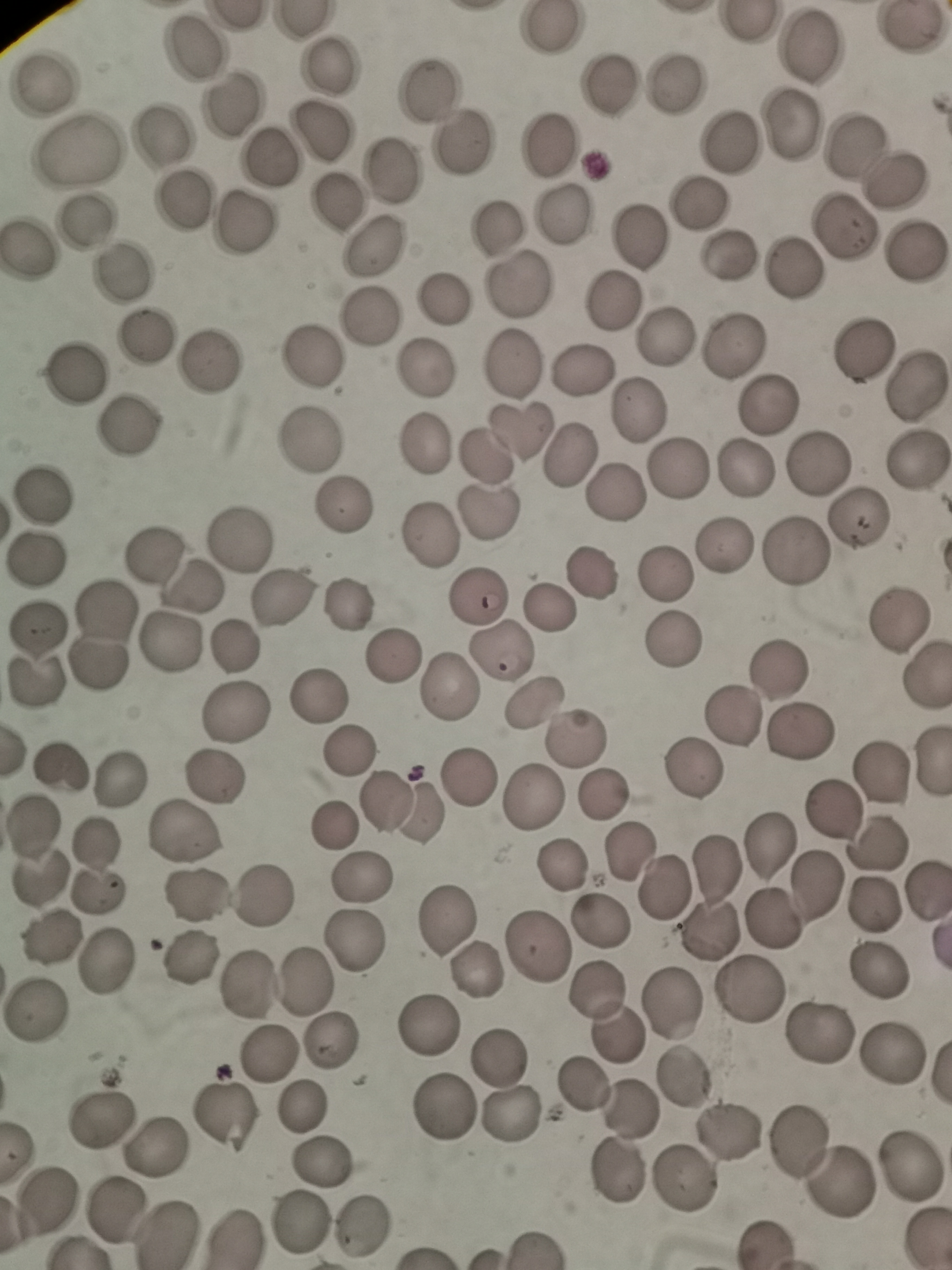 Approximate centers as [x, y] in pixels. Cell locations: [550, 29], [904, 32], [811, 46], [190, 48], [329, 62], [607, 79], [678, 83], [47, 86], [431, 89], [230, 105], [791, 122], [320, 129], [163, 139], [856, 140], [459, 141], [729, 142], [550, 146], [81, 153], [273, 156], [389, 169], [896, 181], [185, 201], [337, 202], [699, 204], [567, 216], [246, 220], [85, 222], [846, 228], [497, 231], [643, 236], [376, 245], [29, 249], [915, 249], [731, 253], [791, 268], [122, 271], [520, 283], [442, 300], [613, 302], [367, 318], [667, 335], [144, 336], [738, 344], [862, 344], [310, 355], [515, 361], [209, 366], [428, 368], [584, 370], [74, 374], [916, 383], [772, 402], [640, 406], [130, 426], [521, 429], [426, 443], [309, 446], [483, 453], [569, 454], [817, 459], [916, 461], [744, 464], [675, 471], [619, 493], [40, 494], [346, 508], [489, 511], [855, 518], [432, 536], [240, 539], [727, 542], [793, 550], [153, 551], [38, 555], [591, 573], [665, 575], [195, 585], [286, 596], [479, 596], [349, 602], [551, 607], [894, 624], [38, 631], [101, 634], [170, 641], [672, 641], [238, 643], [500, 652], [391, 654], [781, 673], [926, 674], [35, 685], [451, 686], [324, 691], [531, 701], [236, 711], [736, 719], [799, 732], [575, 738], [350, 748], [932, 759], [62, 762], [883, 768], [694, 773], [127, 775], [212, 775], [470, 782], [602, 793], [389, 800], [531, 802], [833, 809], [331, 826], [32, 829], [184, 833], [98, 842], [879, 842], [769, 843], [629, 850], [562, 864], [718, 867], [365, 871], [40, 884], [816, 886], [665, 887], [264, 892], [926, 892], [200, 893], [101, 894], [875, 903], [448, 918], [773, 918], [600, 921], [49, 941], [357, 941], [538, 944], [188, 954], [106, 961], [878, 970], [476, 972], [308, 979], [254, 982], [597, 991], [747, 992], [670, 1001], [35, 1007], [431, 1024], [818, 1032], [612, 1033], [334, 1037], [892, 1049], [271, 1055], [497, 1056], [683, 1075], [581, 1083], [304, 1108], [441, 1108], [629, 1111], [511, 1114], [103, 1116], [223, 1118], [729, 1131], [797, 1135], [156, 1142], [321, 1161], [910, 1164], [610, 1174], [837, 1180], [685, 1183], [46, 1196], [113, 1210], [300, 1221], [358, 1228], [168, 1229], [236, 1236]. Thin blood smear. Giemsa stain. Acquired by smartphone through the microscope eyepiece. One field from this slide. Image is 952×1270 pixels.